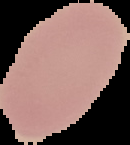

malaria status = uninfected
preparation = thin blood smear
image size = 130×145 pixels
image type = segmented cell region with the area outside set to black